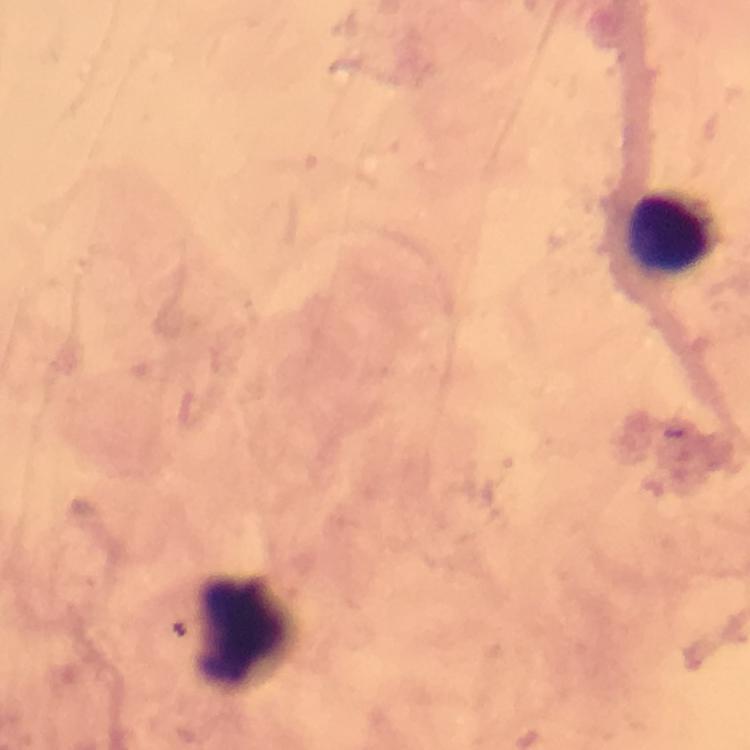

{
  "malaria_parasites": "none detected",
  "immersion_oil": "used",
  "cropped_from": "a single field of view",
  "magnification": "100x",
  "leukocyte_locations": "approximate centers as [x, y] in pixels: [667, 237], [247, 635]",
  "image_size": "750×750 pixels",
  "context": "from a diagnostic examination for malaria",
  "preparation": "thick blood film",
  "stain": "Giemsa",
  "capture": "smartphone camera through the microscope"
}